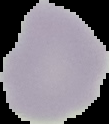 Malaria status: uninfected. The area outside the segmented cell region is set to black. Image is 109×124 pixels. From a thin blood film.